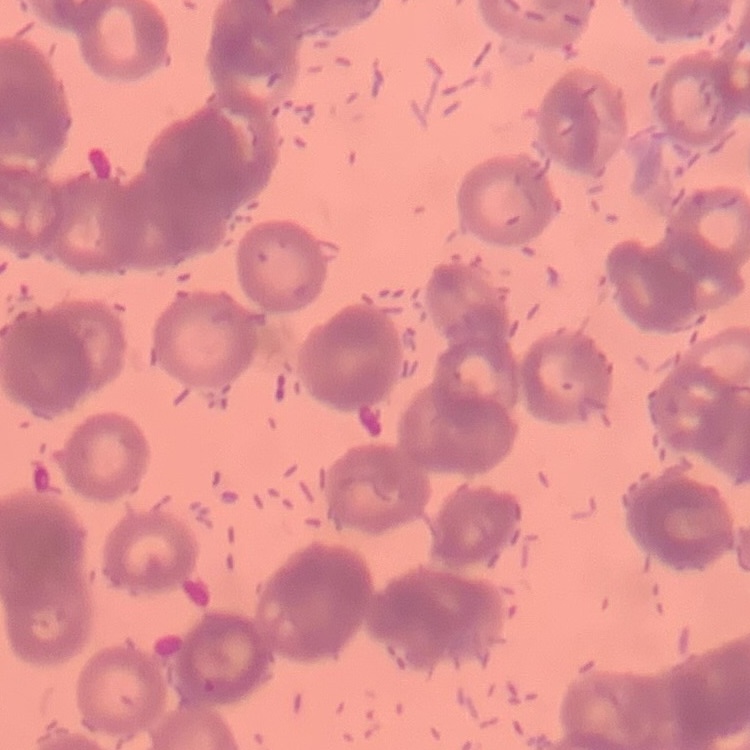

red blood cell morphology = rouleaux formation
stain = Field's or Giemsa
image type = one tile cut from a larger photomicrograph
preparation = thin blood film